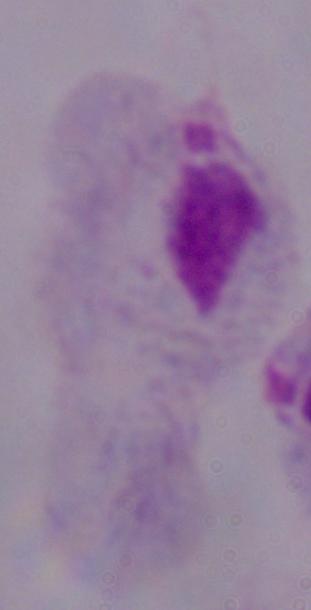
Summary:
  - Identification: trichomonad
  - Magnification: 1000x
  - Modality: micrograph